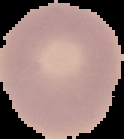

image_size: 124×139 pixels
image_type: cell region segmented out of the field of view; surrounding area masked to black
preparation: thin blood film
malaria_status: uninfected